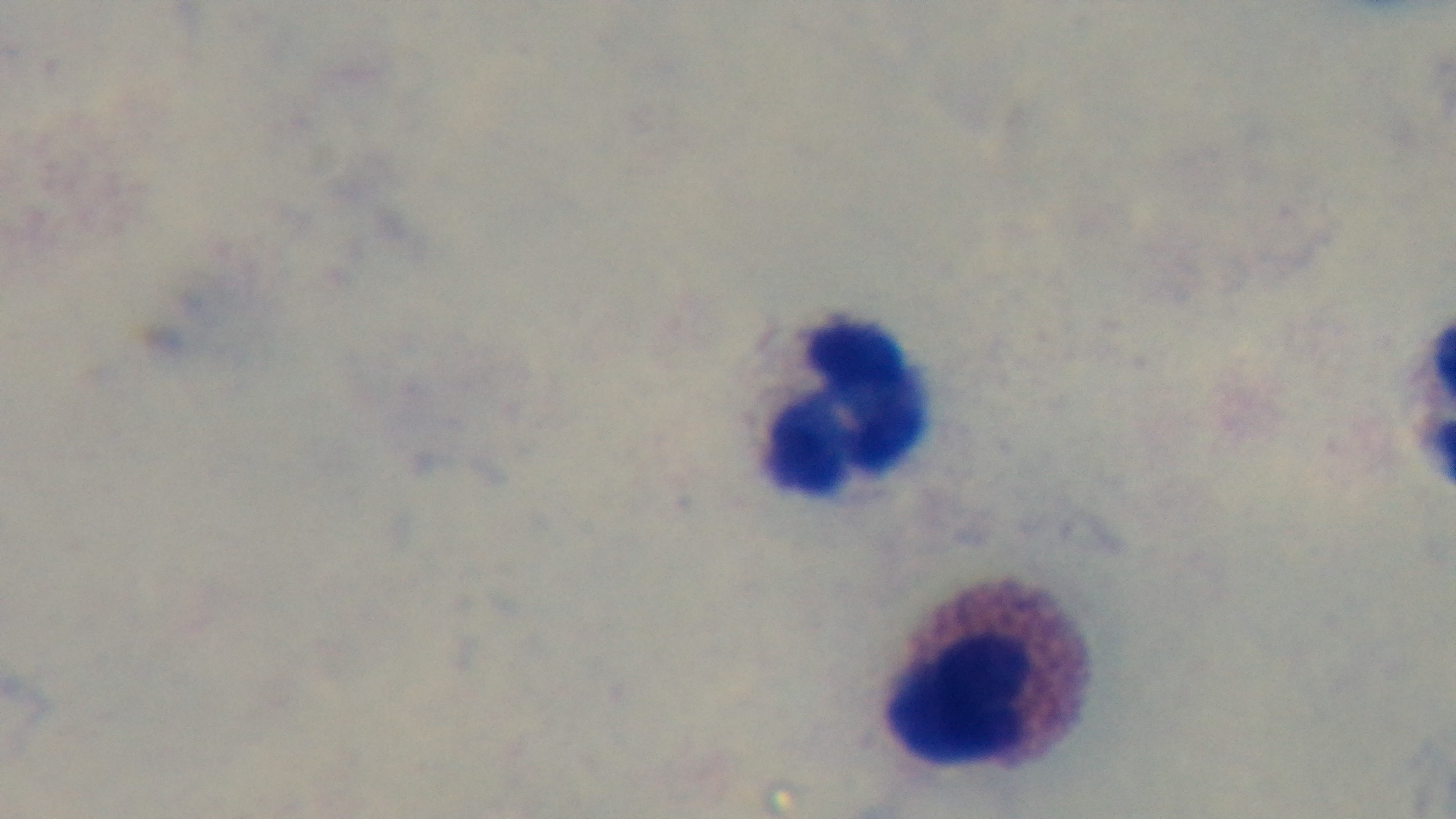

Summary:
  - Preparation: thick blood film
  - Objective: 100x oil immersion
  - Field of view: one from the slide
  - Capture: mounted 4K digital camera
  - Modality: light microscopy
  - Malaria status: uninfected
  - Stain: Giemsa